State the preparation type.
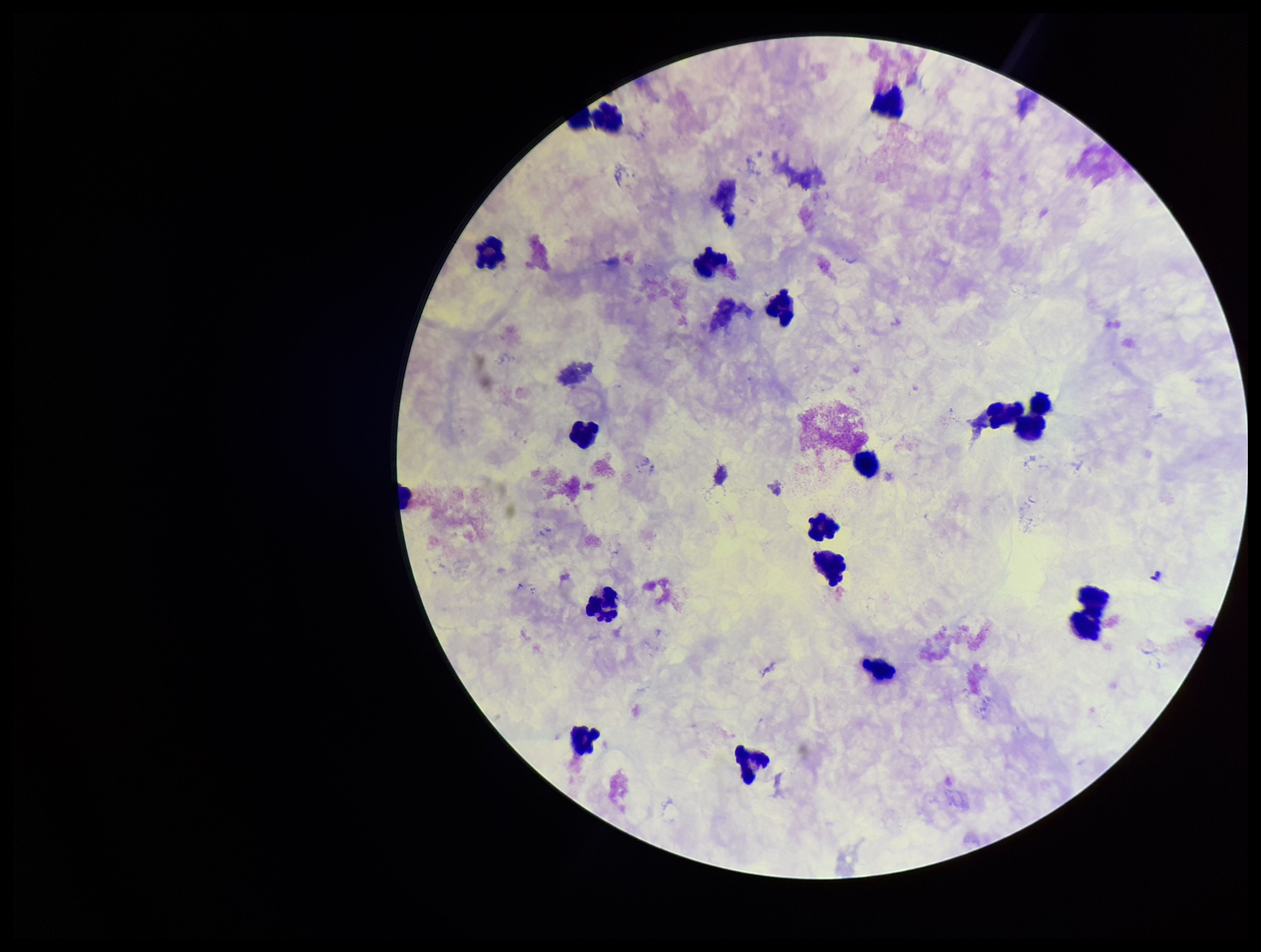
A thick smear.

parasite count = 0
field of view = one from this slide
Plasmodium parasites = none seen
leukocyte count = 17
capture = smartphone photograph through the microscope eyepiece
stain = Giemsa
patient malaria status = negative
image size = 1261×952 pixels